State which parasite is depicted.
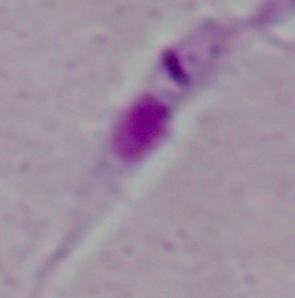
This is Leishmania.

1000x magnification. Micrograph.